Give the extent of all Plasmodium ovale-infected red blood cells.
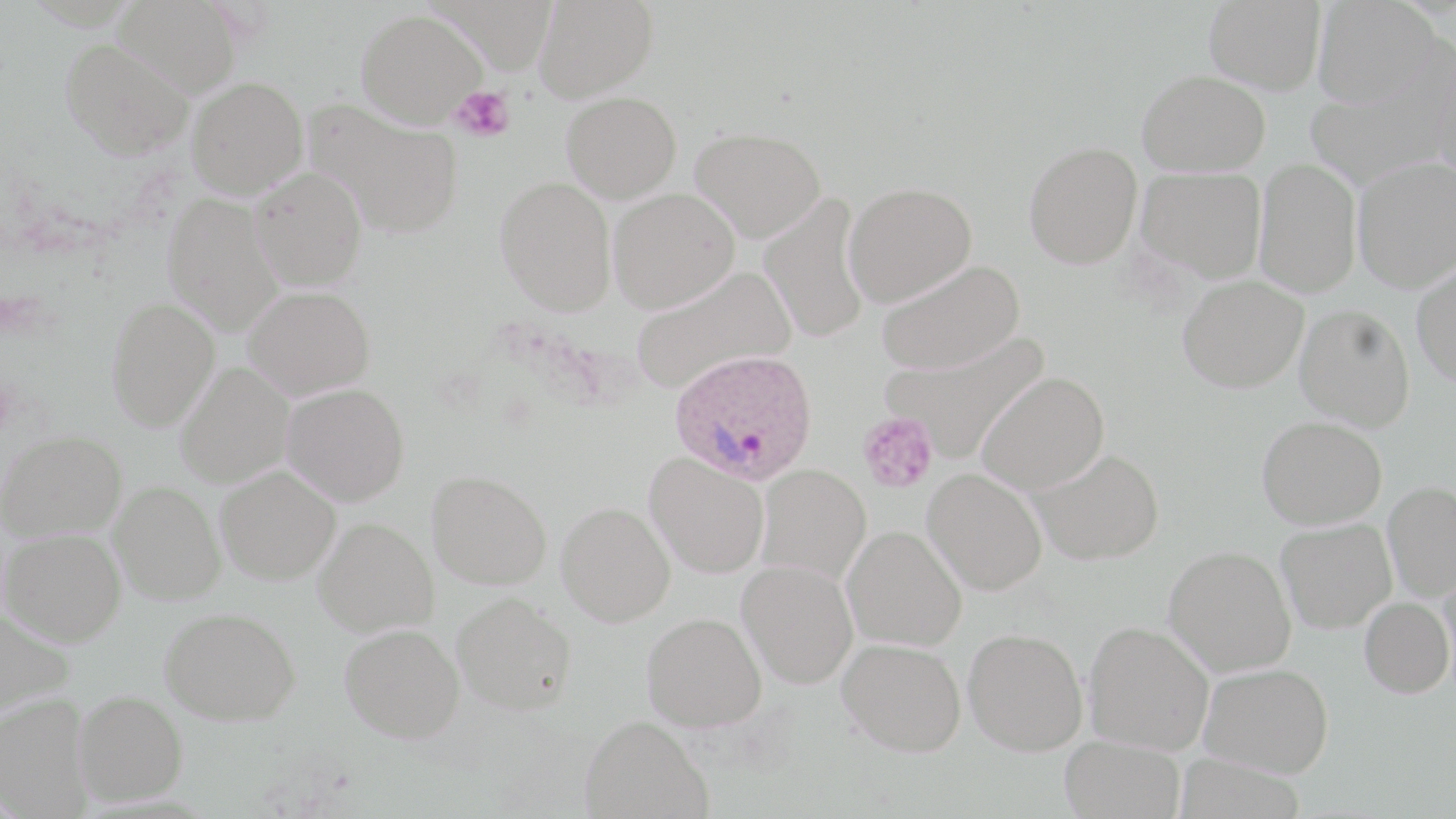

Approximate bounding boxes as (x1,y1)-(x2,y2) corner pairs in pixels.
Plasmodium ovale-infected red blood cells: (670,349)-(819,484).

Summary:
  - Uninfected red blood cell locations: (114,0)-(242,98), (431,0)-(558,72), (534,0)-(658,102), (1204,0)-(1326,94), (1312,0)-(1442,107), (356,9)-(487,127), (60,38)-(193,159), (1304,66)-(1456,186), (1137,69)-(1270,176), (187,76)-(308,198), (561,91)-(681,202), (306,98)-(464,238), (691,127)-(826,242), (1023,141)-(1143,269), (1353,156)-(1456,292), (1254,158)-(1361,298), (250,166)-(368,291), (1136,166)-(1266,281), (495,175)-(616,316), (844,182)-(977,306), (608,187)-(739,312), (163,192)-(284,336), (759,195)-(871,344), (875,259)-(1024,376), (1412,259)-(1456,386), (630,266)-(795,394), (1177,274)-(1308,392), (243,285)-(375,400), (105,298)-(219,431), (1295,304)-(1415,431), (883,330)-(1050,462), (175,362)-(294,488), (977,372)-(1109,494), (282,384)-(409,506), (1257,416)-(1386,529), (0,429)-(127,541), (1033,449)-(1164,565), (645,451)-(769,579), (756,464)-(871,585), (215,465)-(341,584), (426,469)-(552,590), (923,469)-(1047,595), (109,481)-(225,604), (1383,482)-(1456,600), (556,501)-(675,626), (314,517)-(438,637), (1276,518)-(1396,632), (842,526)-(966,651), (2,528)-(126,646), (1165,545)-(1297,676), (737,560)-(858,688), (1437,570)-(1455,689), (453,591)-(577,715), (1359,596)-(1454,698), (0,606)-(75,717), (160,607)-(302,725), (642,612)-(767,731), (1084,621)-(1214,754), (339,623)-(465,743), (964,627)-(1088,755), (837,637)-(966,756), (1200,663)-(1334,776), (74,690)-(188,806), (0,692)-(93,817), (580,715)-(713,819), (1060,735)-(1185,819)
  - Platelet locations: (449,86)-(516,143), (857,412)-(939,494)
  - Slide-level diagnosis: Plasmodium ovale
  - Modality: optical microscopy
  - Magnification: 1000x
  - Preparation: thin blood film
  - Stain: May-Grünwald-Giemsa
  - Field of view: single
  - Image size: 1456×819 pixels